Assess for malaria.
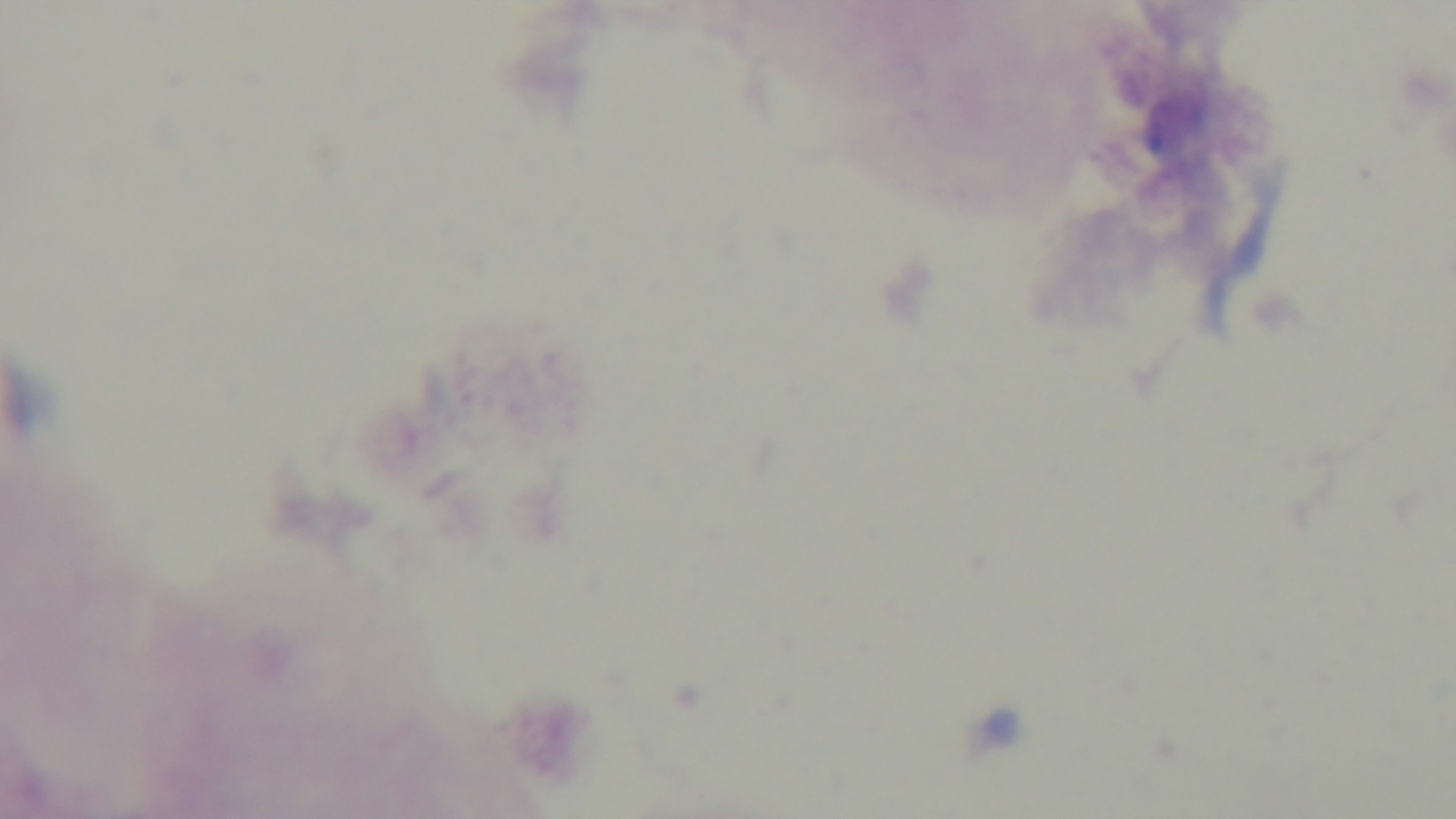

Negative.

Oil-immersion objective, 100x. Preparation: thick blood film. One field from the slide. Mounted 4K digital camera. Photomicrograph. Giemsa stain.